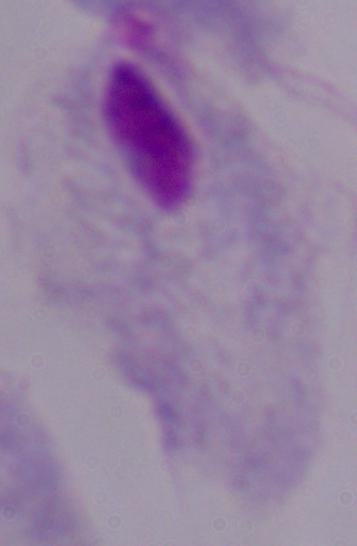

Summary:
  - Modality: photomicrograph
  - Identification: trichomonad
  - Magnification: 1000x